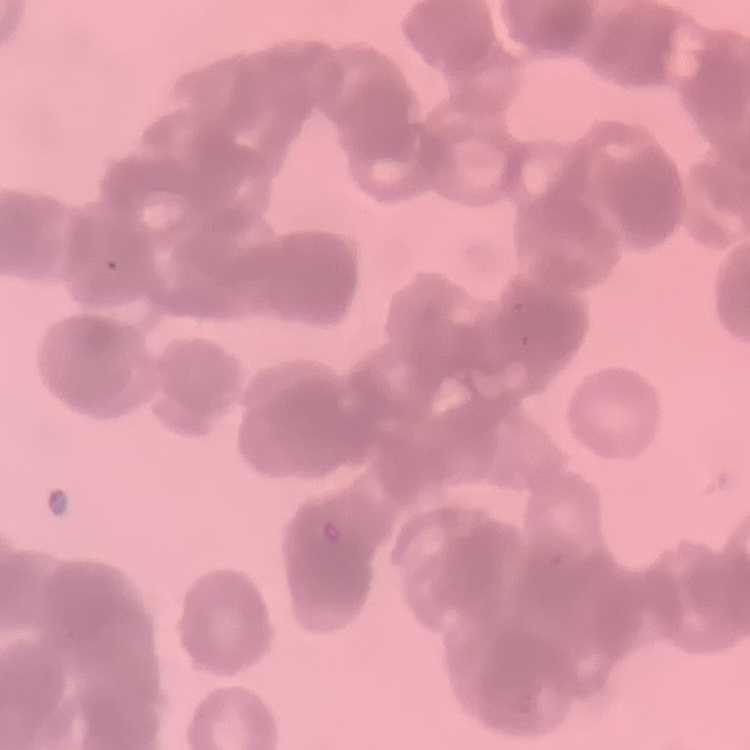
Summary:
  - Red blood cell morphology: rouleaux formation
  - Preparation: thin blood film
  - Image type: square crop of a larger photomicrograph
  - Stain: Field's or Giemsa